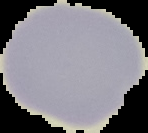

image type = segmented cell region with the area outside set to black
preparation = thin blood film
malaria status = uninfected
image size = 148×133 pixels